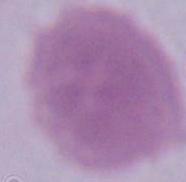
Summary:
  - Magnification: 1000x
  - Modality: photomicrograph
  - Identification: red blood cell